Report the malaria status of this cell.
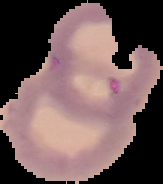

Parasitized.

From a thin blood film. Cell region segmented out of the field of view; the surrounding area is masked to black. Image is 163×184 pixels.